Evaluate for parasitized red blood cells.
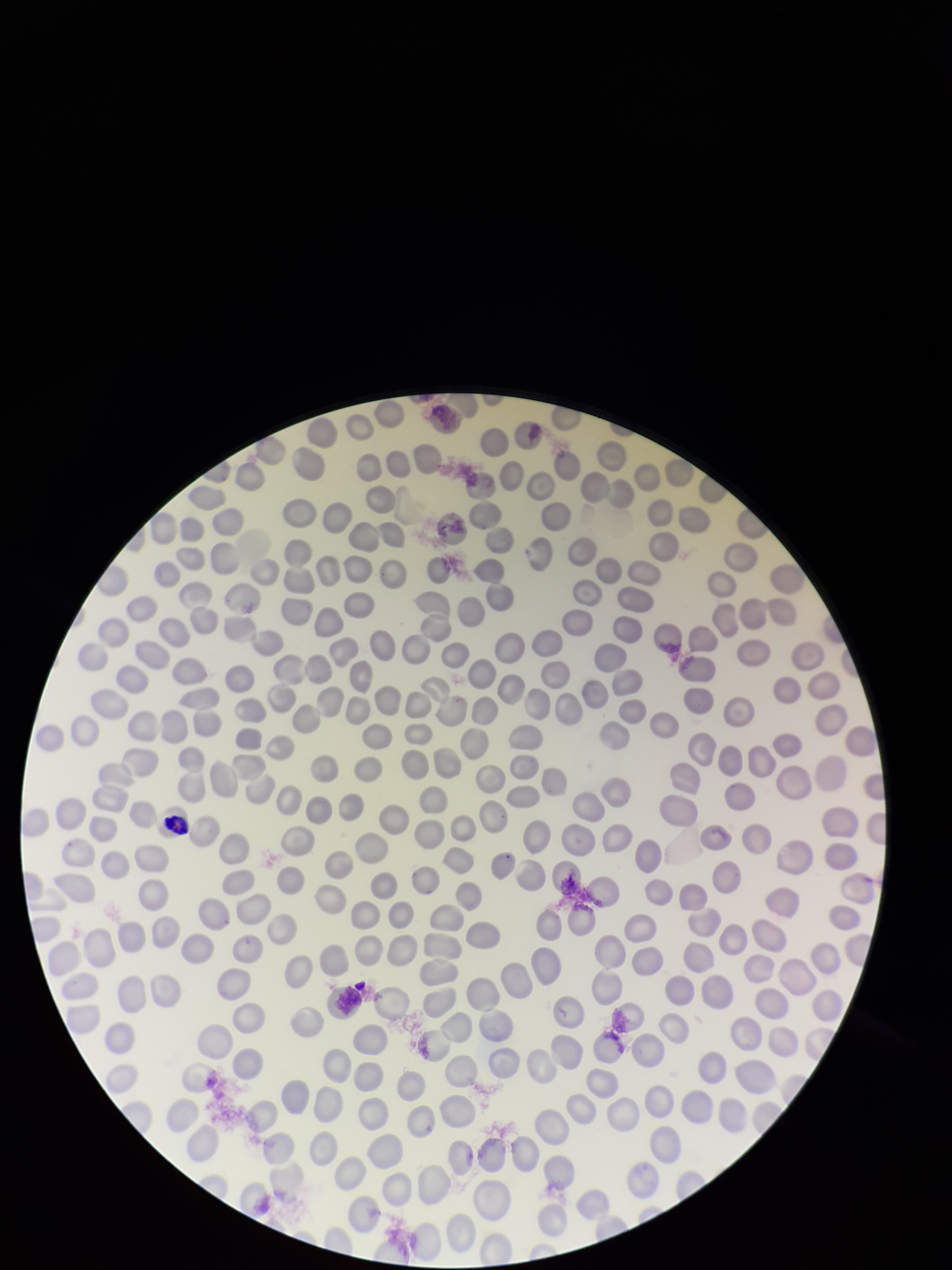
None seen.

image_size: 952×1270 pixels
preparation: thin smear
parasitized_red_blood_cell_count: 0
capture: smartphone photograph through the microscope eyepiece
patient_malaria_status: negative
field_of_view: single
red_blood_cell_count: 264
stain: Giemsa